Locate every leukocyte (white blood cell).
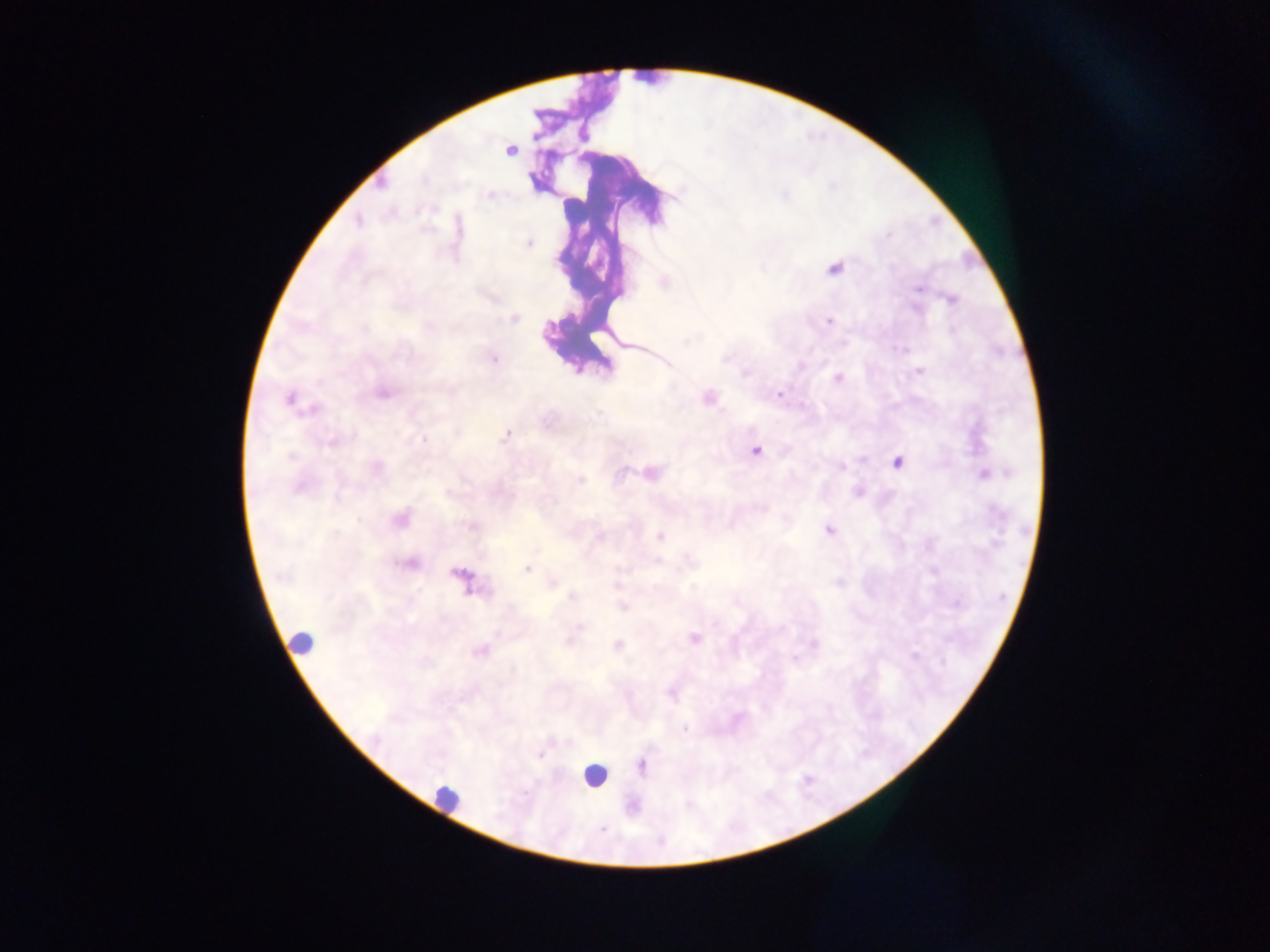

Approximate centers as {x, y} in pixels.
Leukocytes: {593, 779}.

preparation = thick blood smear
field of view = single
capture = mobile-phone photograph through a microscope
country = Ghana
image size = 1270×952 pixels
malaria parasite locations = approximate centers as {x, y} in pixels: {583, 135}, {711, 151}, {511, 152}, {490, 195}, {782, 196}, {431, 207}, {358, 223}, {887, 235}, {528, 243}, {557, 261}, {836, 266}, {601, 269}, {916, 287}, {619, 295}, {953, 299}, {513, 319}, {830, 321}, {365, 327}, {685, 341}, {627, 345}, {901, 349}, {726, 359}, {495, 360}, {920, 371}, {746, 373}, {837, 377}, {385, 393}, {450, 393}, {781, 393}, {707, 398}, {289, 400}, {316, 408}, {598, 415}, {506, 434}, {334, 439}, {422, 440}, {329, 445}, {755, 450}, {289, 456}, {897, 462}, {377, 468}, {842, 468}, {621, 470}, {653, 473}, {982, 474}, {580, 480}, {858, 493}, {400, 518}, {359, 521}, {470, 527}, {829, 530}, {598, 535}, {659, 535}, {657, 561}, {411, 563}, {528, 568}, {455, 573}, {281, 576}, {462, 578}, {553, 582}, {617, 582}, {470, 591}, {570, 596}, {623, 607}, {577, 629}, {496, 633}, {572, 634}, {693, 638}, {570, 641}, {299, 642}, {617, 645}, {815, 645}, {479, 652}, {914, 655}, {795, 658}, {541, 757}, {446, 796}